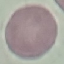 Malaria status: uninfected. Thin blood film. Acquired by smartphone through the microscope eyepiece. Giemsa stain. Automatically extracted cell patch, resized to 64 × 64 pixels.